Identify the parasite.
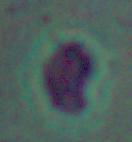

This is Leishmania.

{
  "modality": "micrograph",
  "magnification": "1000x"
}